Assess this cell for malaria.
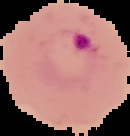
Parasitized.

image size = 130×136 pixels
preparation = thin blood smear
image type = segmented cell region with the area outside set to black